Give the position of every Plasmodium parasite and every leukocyte.
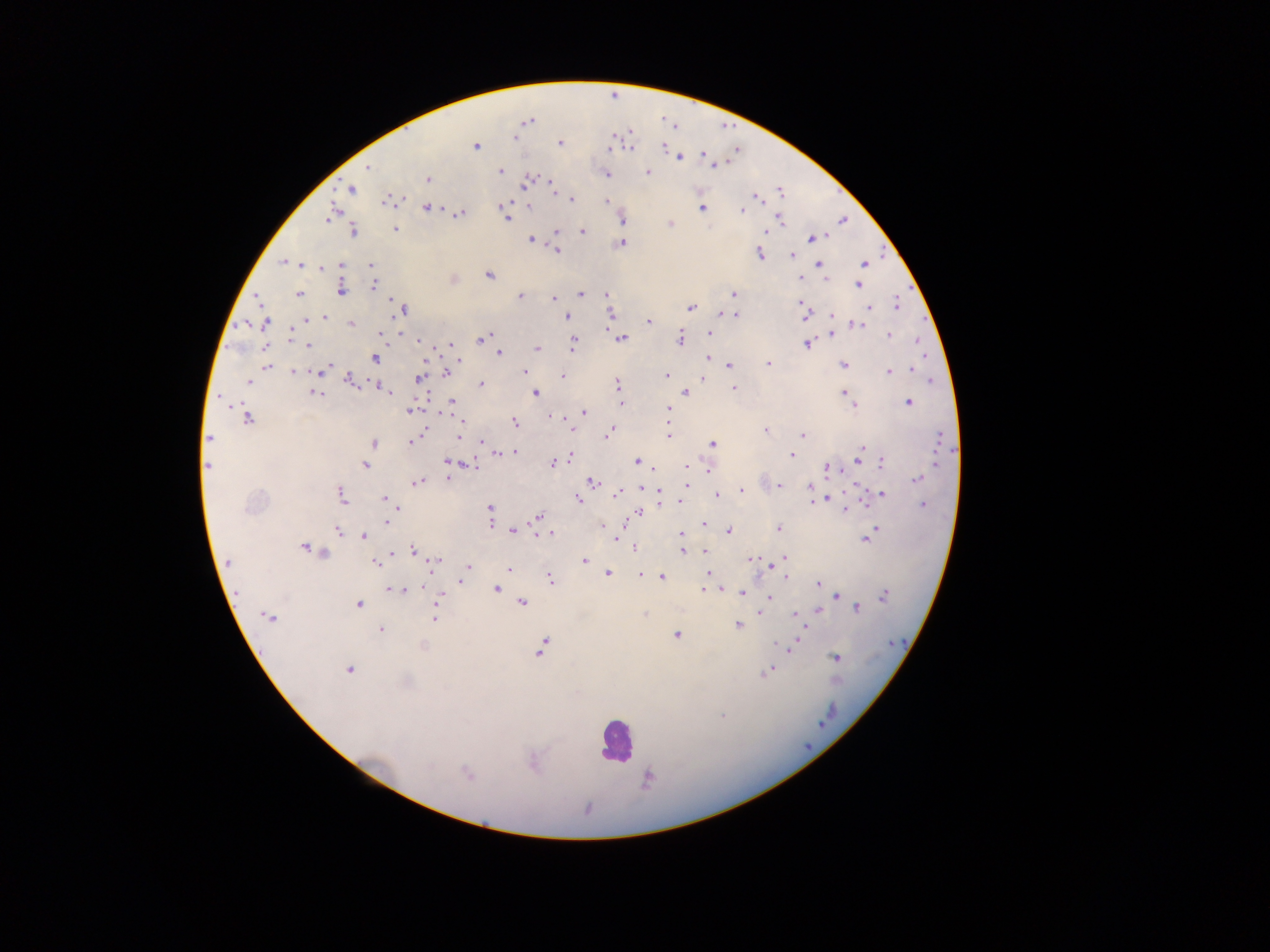
Approximate centers as [x, y] in pixels.
Plasmodium parasites: [516, 138], [560, 139], [476, 146], [663, 146], [629, 148], [610, 149], [679, 158], [714, 166], [367, 167], [501, 172], [647, 172], [607, 174], [427, 179], [531, 179], [526, 182], [551, 185], [351, 189], [553, 189], [781, 192], [755, 198], [387, 200], [572, 200], [607, 202], [502, 205], [529, 206], [426, 208], [701, 208], [742, 210], [461, 213], [330, 215], [779, 218], [507, 219], [621, 220], [670, 223], [395, 228], [766, 230], [354, 231], [556, 231], [582, 232], [813, 238], [531, 240], [621, 243], [557, 251], [760, 254], [791, 254], [284, 261], [864, 264], [342, 265], [819, 265], [371, 266], [322, 268], [488, 275], [800, 277], [826, 279], [374, 284], [858, 285], [341, 290], [581, 294], [733, 294], [298, 295], [607, 295], [520, 296], [256, 297], [553, 299], [801, 303], [896, 304], [690, 307], [869, 307], [403, 309], [867, 311], [726, 314], [611, 315], [735, 315], [832, 315], [566, 316], [805, 316], [324, 317], [308, 319], [266, 322], [649, 322], [351, 324], [859, 325], [379, 333], [710, 333], [831, 334], [889, 335], [485, 338], [622, 339], [681, 339], [917, 341], [806, 344], [309, 346], [450, 346], [572, 347], [537, 349], [499, 353], [375, 358], [707, 358], [459, 360], [768, 364], [843, 365], [268, 366], [729, 366], [326, 370], [911, 370], [525, 371], [888, 371], [294, 372], [319, 372], [446, 373], [562, 376], [666, 376], [703, 377], [419, 379], [351, 381], [248, 382], [482, 384], [618, 384], [381, 387], [733, 387], [387, 391], [315, 393], [535, 393], [686, 393], [844, 393], [848, 398], [452, 402], [620, 402], [909, 402], [854, 405], [668, 409], [410, 411], [584, 412], [551, 417], [248, 419], [460, 421], [515, 422], [572, 429], [766, 430], [610, 431], [803, 434], [608, 435], [668, 435], [209, 437], [459, 437], [939, 439], [410, 442], [482, 442], [374, 444], [713, 444], [492, 448], [862, 449], [512, 452], [499, 453], [792, 455], [570, 456], [861, 460], [638, 461], [447, 462], [552, 463], [882, 463], [365, 465], [471, 465], [686, 466], [207, 467], [828, 468], [654, 469], [709, 469], [448, 479], [917, 479], [416, 482], [592, 483], [686, 485], [779, 485], [811, 487], [642, 489], [741, 491], [660, 493], [616, 494], [882, 494], [341, 495], [718, 495], [829, 496], [384, 498], [578, 499], [814, 501], [680, 502], [865, 502], [923, 506], [490, 509], [846, 509], [395, 510], [640, 512], [538, 517], [386, 522], [704, 524], [491, 525], [778, 528], [513, 530], [729, 531], [337, 532], [874, 532], [550, 534], [681, 534], [364, 536], [614, 538], [866, 538], [303, 547], [634, 548], [413, 550], [705, 551], [683, 552], [322, 553], [393, 553], [751, 558], [784, 558], [583, 561], [229, 562], [375, 563], [434, 564], [775, 564], [467, 568], [509, 570], [608, 573], [708, 573], [640, 575], [785, 575], [662, 578], [550, 579], [460, 580], [818, 585], [396, 589], [497, 589], [704, 589], [711, 590], [718, 590], [742, 593], [837, 596], [884, 596], [769, 597], [439, 599], [523, 603], [358, 605], [436, 609], [857, 609], [818, 611], [759, 613], [645, 614], [796, 615], [269, 618], [435, 618], [737, 626], [380, 630], [677, 635], [795, 643], [779, 645], [423, 646], [788, 647], [542, 648], [835, 657], [349, 670], [767, 672], [407, 682], [722, 716], [532, 765], [466, 773], [647, 780].
Leukocytes: [615, 740].

Image is 1270×952 pixels. Sample from Ghana. Thick blood film. Single field of view. Mobile-phone photograph taken through the microscope.